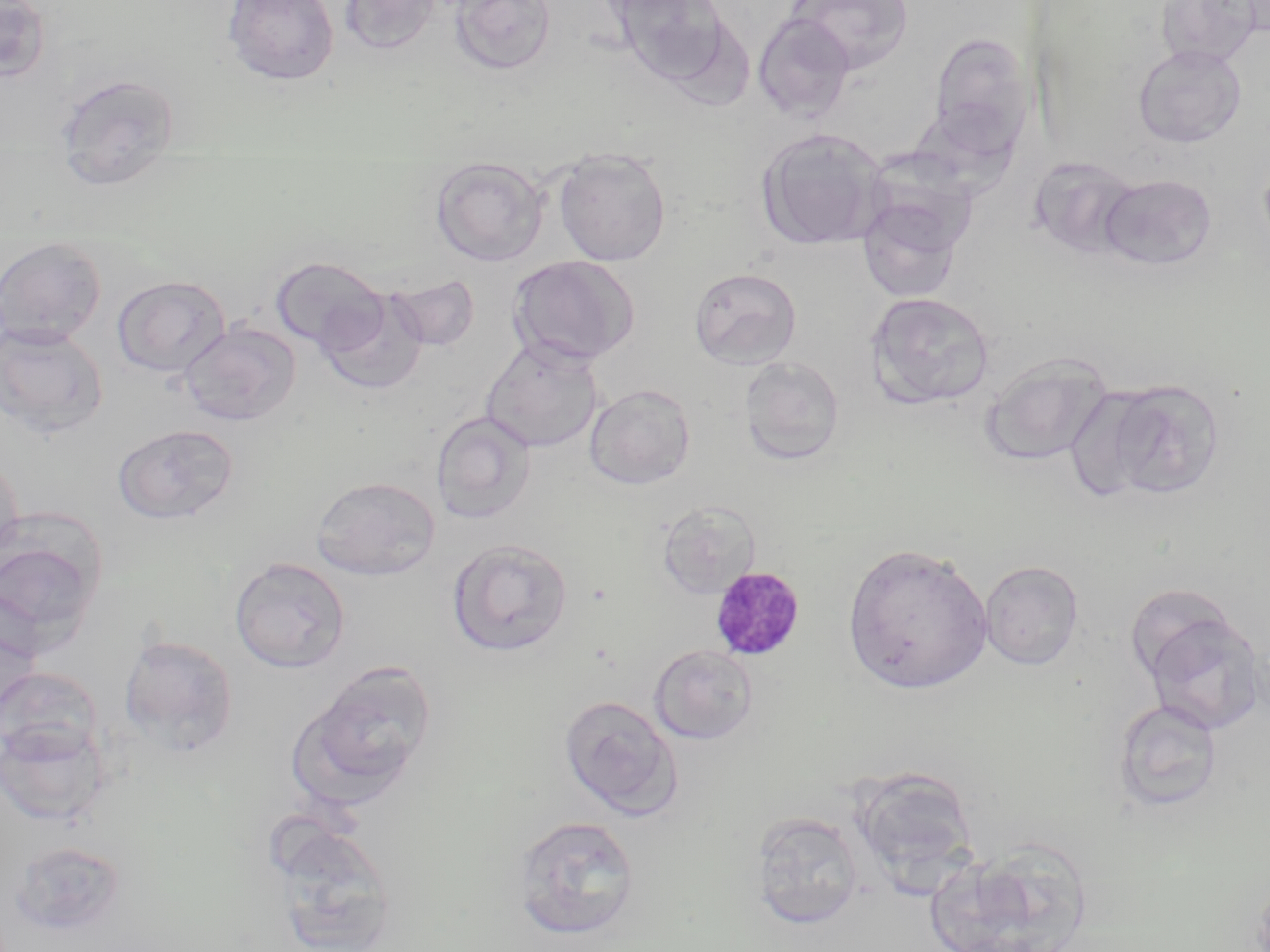

Approximate bounding boxes as named x1/y1/x2/y2 corners in pixels. Plasmodium malariae-infected red blood cell locations: (x1=709, y1=566, x2=806, y2=661). Uninfected red blood cell locations: (x1=223, y1=0, x2=340, y2=86), (x1=339, y1=0, x2=442, y2=55), (x1=449, y1=0, x2=558, y2=77), (x1=612, y1=0, x2=733, y2=85), (x1=787, y1=0, x2=912, y2=75), (x1=1155, y1=0, x2=1265, y2=69), (x1=0, y1=1, x2=52, y2=83), (x1=753, y1=12, x2=856, y2=122), (x1=928, y1=31, x2=1034, y2=158), (x1=1133, y1=44, x2=1247, y2=147), (x1=54, y1=74, x2=181, y2=191), (x1=756, y1=127, x2=888, y2=251), (x1=553, y1=147, x2=672, y2=266), (x1=430, y1=156, x2=549, y2=266), (x1=1029, y1=156, x2=1143, y2=259), (x1=1099, y1=173, x2=1217, y2=271), (x1=854, y1=188, x2=971, y2=304), (x1=0, y1=236, x2=107, y2=348), (x1=507, y1=255, x2=639, y2=366), (x1=270, y1=256, x2=390, y2=355), (x1=688, y1=266, x2=802, y2=369), (x1=386, y1=271, x2=481, y2=352), (x1=112, y1=275, x2=231, y2=377), (x1=315, y1=289, x2=428, y2=396), (x1=864, y1=291, x2=995, y2=410), (x1=178, y1=321, x2=301, y2=426), (x1=0, y1=322, x2=108, y2=439), (x1=481, y1=338, x2=604, y2=453), (x1=980, y1=353, x2=1113, y2=467), (x1=739, y1=356, x2=845, y2=466), (x1=1088, y1=378, x2=1228, y2=501), (x1=584, y1=384, x2=696, y2=490), (x1=431, y1=411, x2=537, y2=524), (x1=113, y1=424, x2=239, y2=524), (x1=0, y1=454, x2=24, y2=567), (x1=311, y1=475, x2=441, y2=580), (x1=656, y1=500, x2=760, y2=599), (x1=0, y1=515, x2=108, y2=650), (x1=447, y1=539, x2=574, y2=657), (x1=842, y1=542, x2=993, y2=695), (x1=229, y1=557, x2=351, y2=673), (x1=979, y1=560, x2=1084, y2=671), (x1=1138, y1=605, x2=1267, y2=734), (x1=118, y1=633, x2=239, y2=758), (x1=648, y1=644, x2=759, y2=745), (x1=299, y1=661, x2=439, y2=799), (x1=0, y1=666, x2=105, y2=766), (x1=559, y1=694, x2=683, y2=819), (x1=1112, y1=698, x2=1224, y2=814), (x1=0, y1=719, x2=112, y2=827), (x1=849, y1=765, x2=980, y2=889), (x1=749, y1=810, x2=866, y2=930), (x1=511, y1=814, x2=640, y2=939), (x1=264, y1=820, x2=401, y2=952), (x1=7, y1=838, x2=128, y2=939), (x1=922, y1=848, x2=1079, y2=952). Slide-level diagnosis: Plasmodium malariae. May-Grünwald-Giemsa-stained preparation. Thin blood smear. Image is 1270×952 pixels. Optical microscopy. 1000x magnification. Single field of view.